Name the blood parasite species.
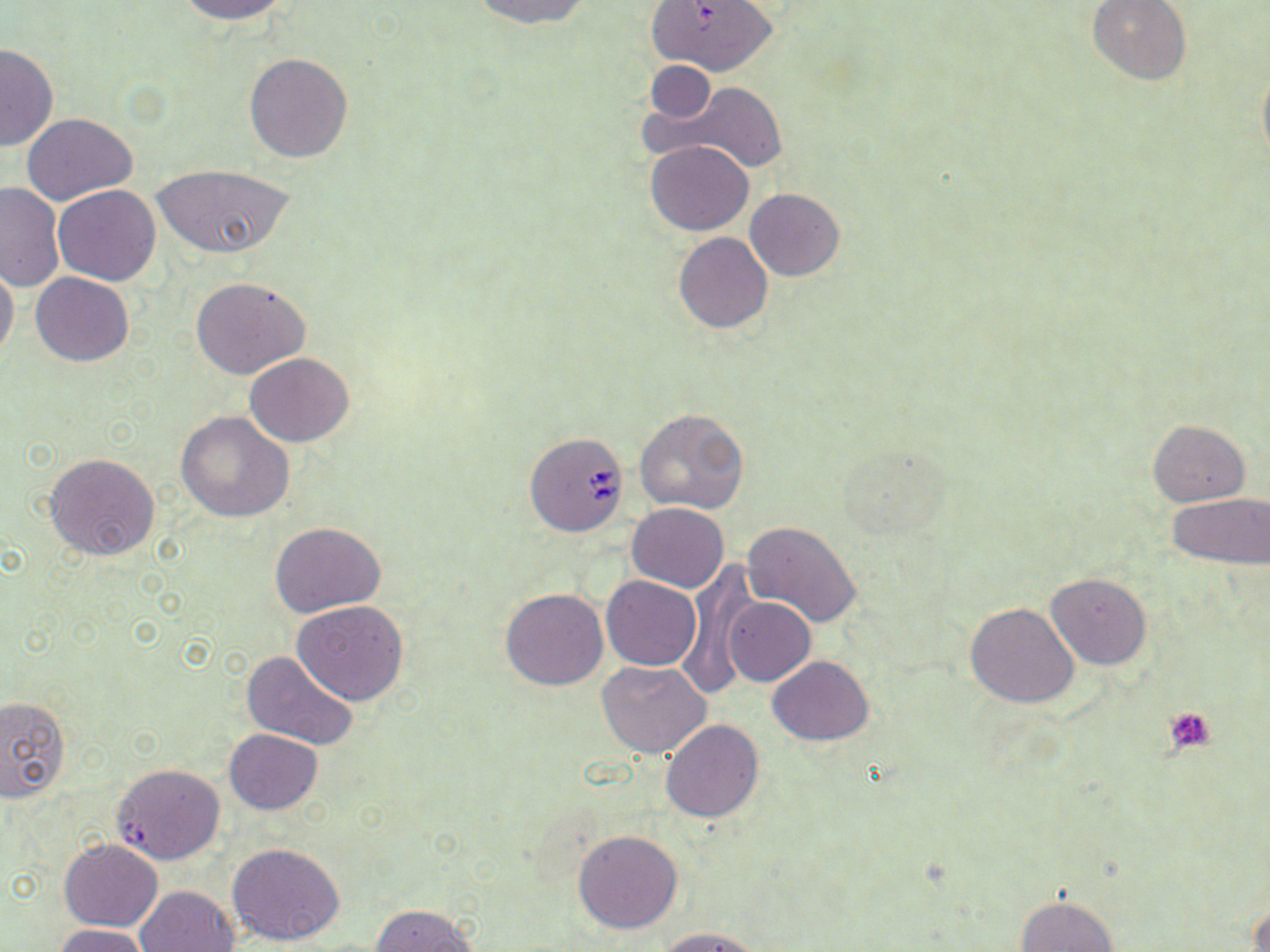

Babesia divergens.

Summary:
  - Coordinate format: approximate bounding boxes as (x1,y1)-(x2,y2) corner pairs in pixels
  - Platelet locations: (1165,705)-(1218,755)
  - Uninfected red blood cell locations: (172,0)-(291,23), (469,0)-(592,28), (650,0)-(776,76), (1087,0)-(1192,85), (0,42)-(58,152), (243,52)-(353,162), (644,61)-(718,124), (1257,64)-(1270,166), (677,82)-(788,175), (22,112)-(137,205), (645,141)-(755,235), (150,162)-(294,260), (0,183)-(64,291), (53,185)-(161,285), (745,188)-(845,280), (673,232)-(773,334), (0,263)-(19,365), (31,272)-(132,366), (191,277)-(310,379), (245,352)-(354,446), (633,407)-(750,516), (176,411)-(294,522), (1148,419)-(1251,506), (831,441)-(958,543), (45,453)-(161,560), (1169,494)-(1270,570), (627,502)-(729,593), (270,520)-(386,616), (740,520)-(864,630), (677,567)-(761,693), (1045,572)-(1151,670), (601,575)-(702,670), (500,586)-(610,691), (722,596)-(815,687), (293,600)-(409,705), (964,602)-(1078,708), (239,650)-(358,749), (767,656)-(874,744), (599,660)-(711,758), (1,695)-(70,803), (660,718)-(764,822), (224,728)-(323,815), (111,763)-(226,865), (573,829)-(683,934), (59,839)-(163,931), (228,842)-(347,946), (135,885)-(239,952), (1016,895)-(1119,952), (1250,900)-(1270,952), (370,903)-(477,952), (52,924)-(155,952), (656,926)-(763,952)
  - Babesia divergens-infected red blood cell locations: (524,431)-(628,537)
  - Magnification: 1000x
  - Stain: May-Grünwald-Giemsa
  - Field of view: one of a larger specimen
  - Image size: 1270×952 pixels
  - Modality: light microscopy
  - Preparation: thin blood film